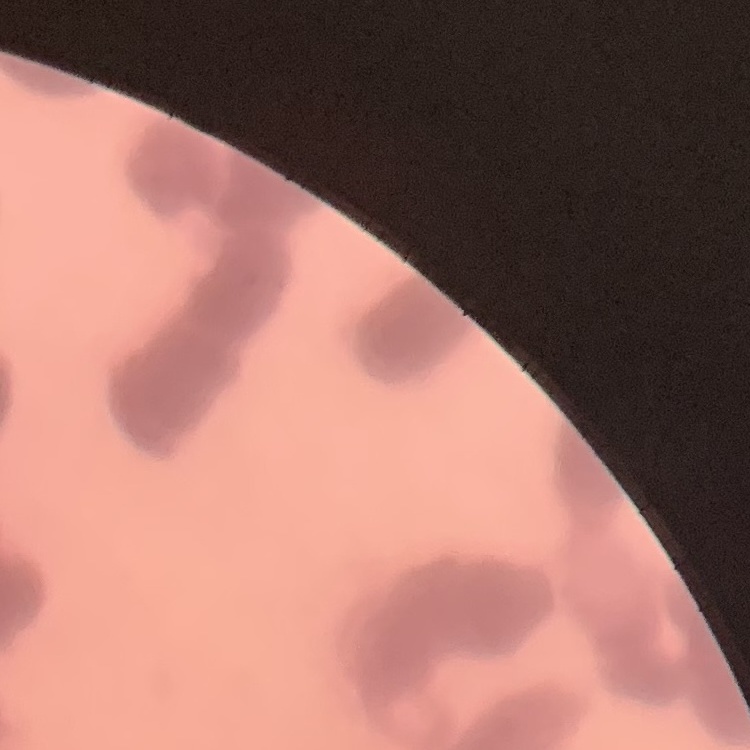 The red blood cells exhibit rouleaux formation. Stained with either Field's or Giemsa. One tile cut from a larger photomicrograph. Thin blood smear.